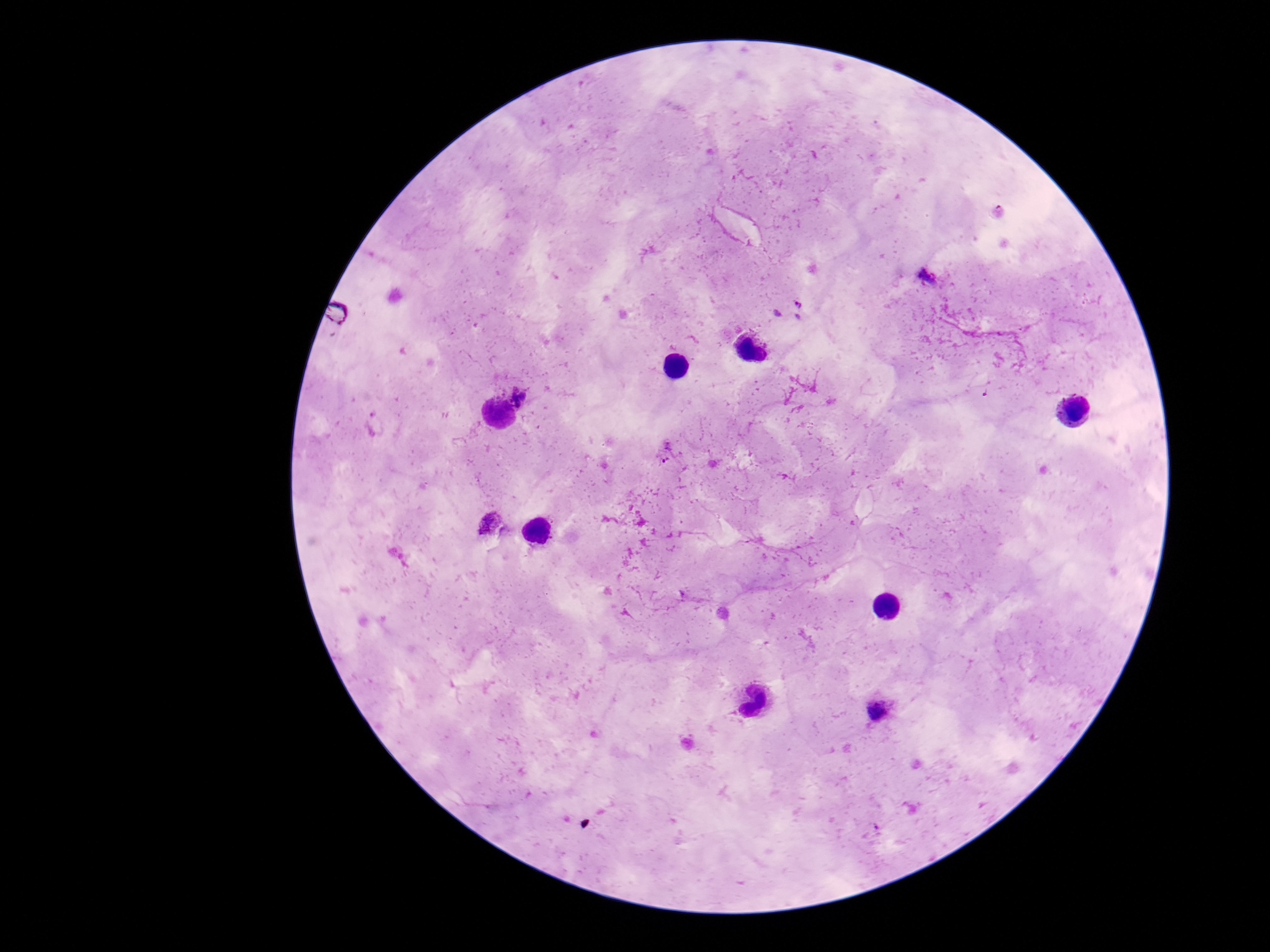
Approximate object centers, in pixels from the top-left corner.
Summary:
  - Plasmodium parasite locations: (x=927, y=277), (x=790, y=310), (x=521, y=392), (x=374, y=425), (x=666, y=451), (x=492, y=524), (x=879, y=710)
  - Magnification: 100x
  - Stain: Giemsa
  - Field of view: single
  - Preparation: thick peripheral-blood smear
  - Image size: 1270×952 pixels
  - Patient malaria status: infected
  - Capture: smartphone camera through the microscope eyepiece